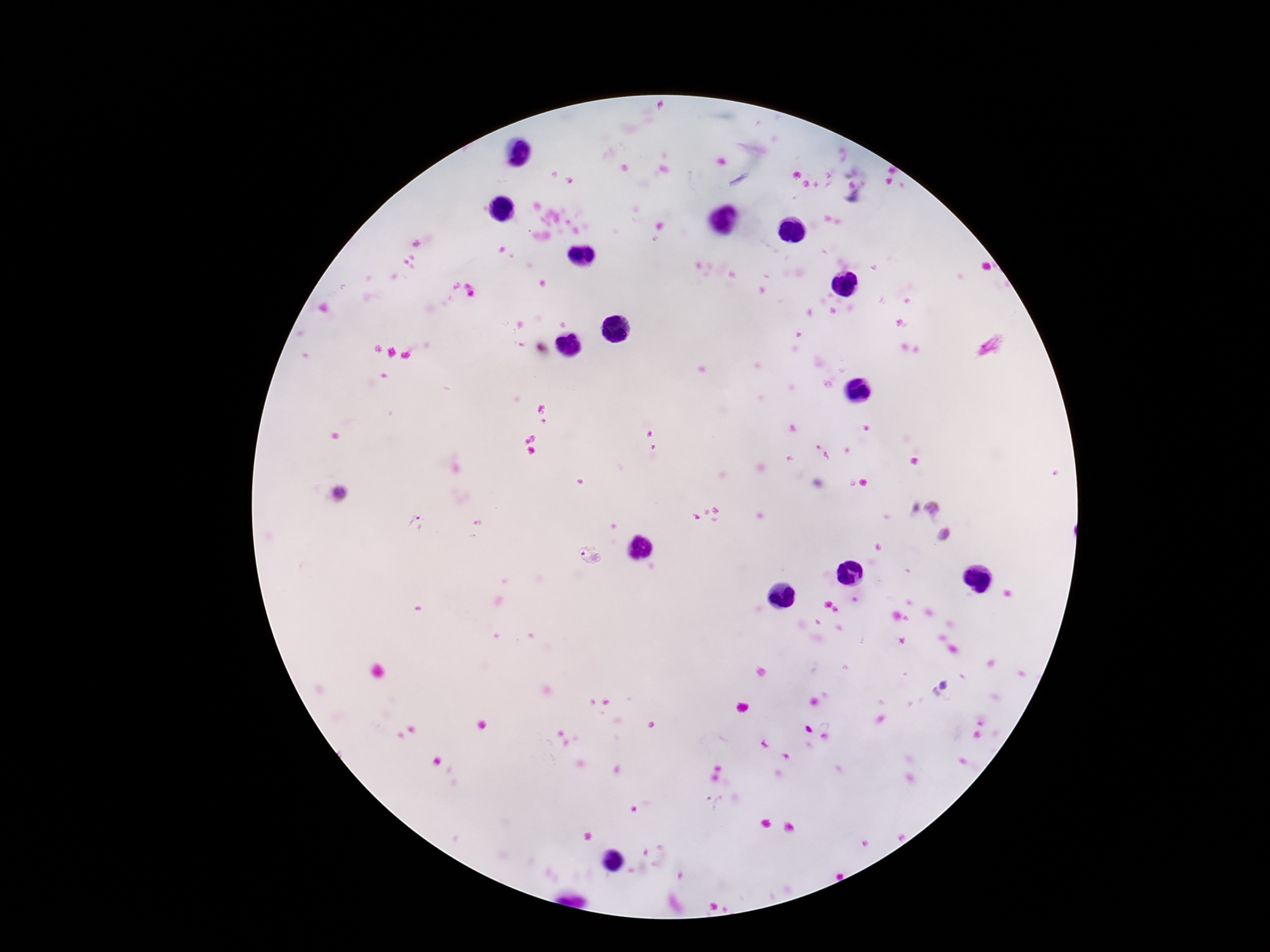
Approximate centers as {x, y} in pixels.
Summary:
  - Plasmodium parasite locations: {931, 508}, {944, 536}, {588, 557}, {944, 684}, {937, 698}, {715, 800}
  - Stain: Giemsa
  - Magnification: 100x
  - Image size: 1270×952 pixels
  - Field of view: single
  - Patient malaria status: positive
  - Preparation: thick blood film
  - Capture: smartphone camera through the microscope eyepiece